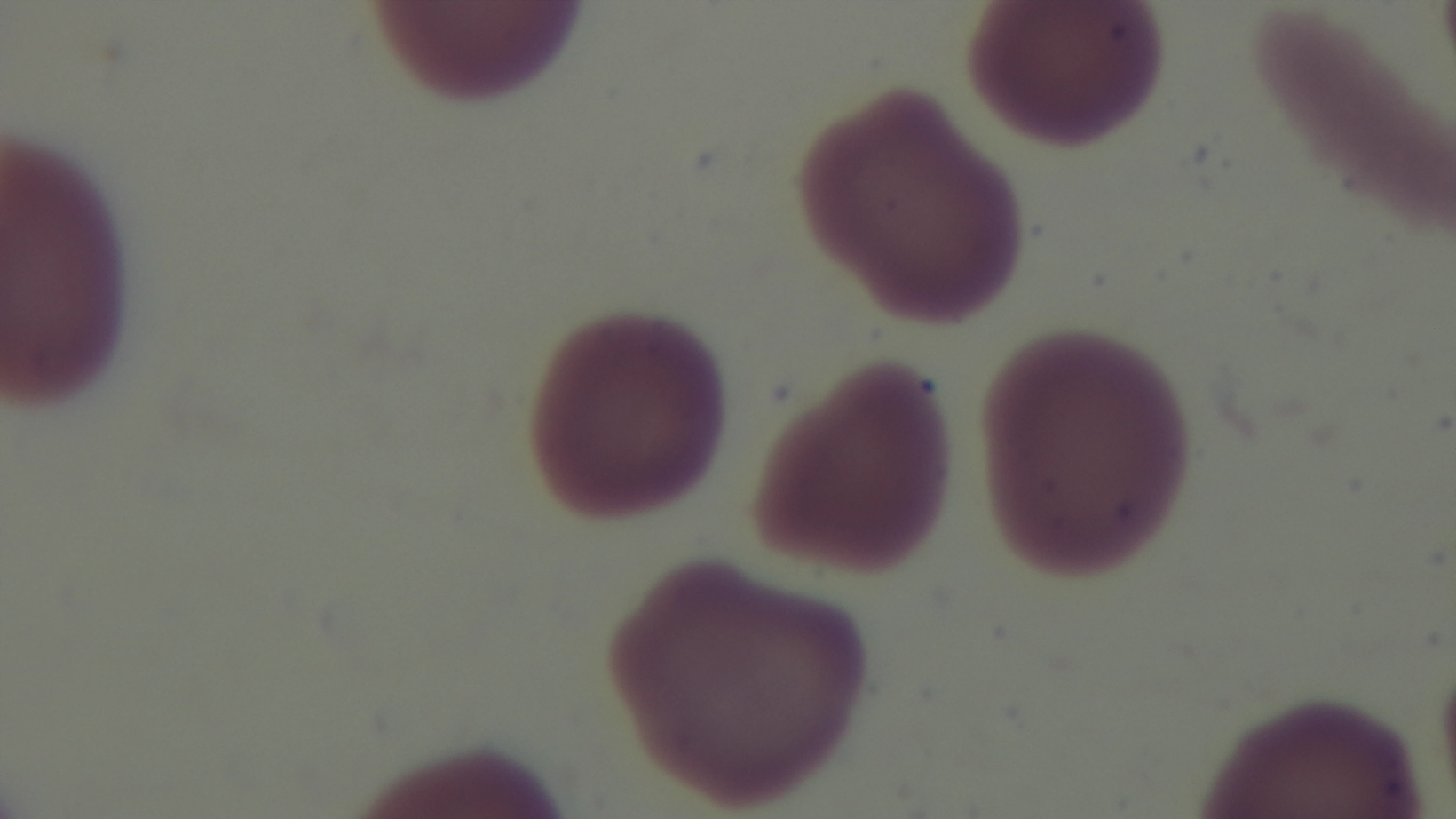

Summary:
  - Preparation: thin smear
  - Capture: mounted 4K digital camera
  - Modality: light microscopy
  - Field of view: single
  - Malaria status: negative
  - Stain: Giemsa
  - Objective: 100x oil immersion